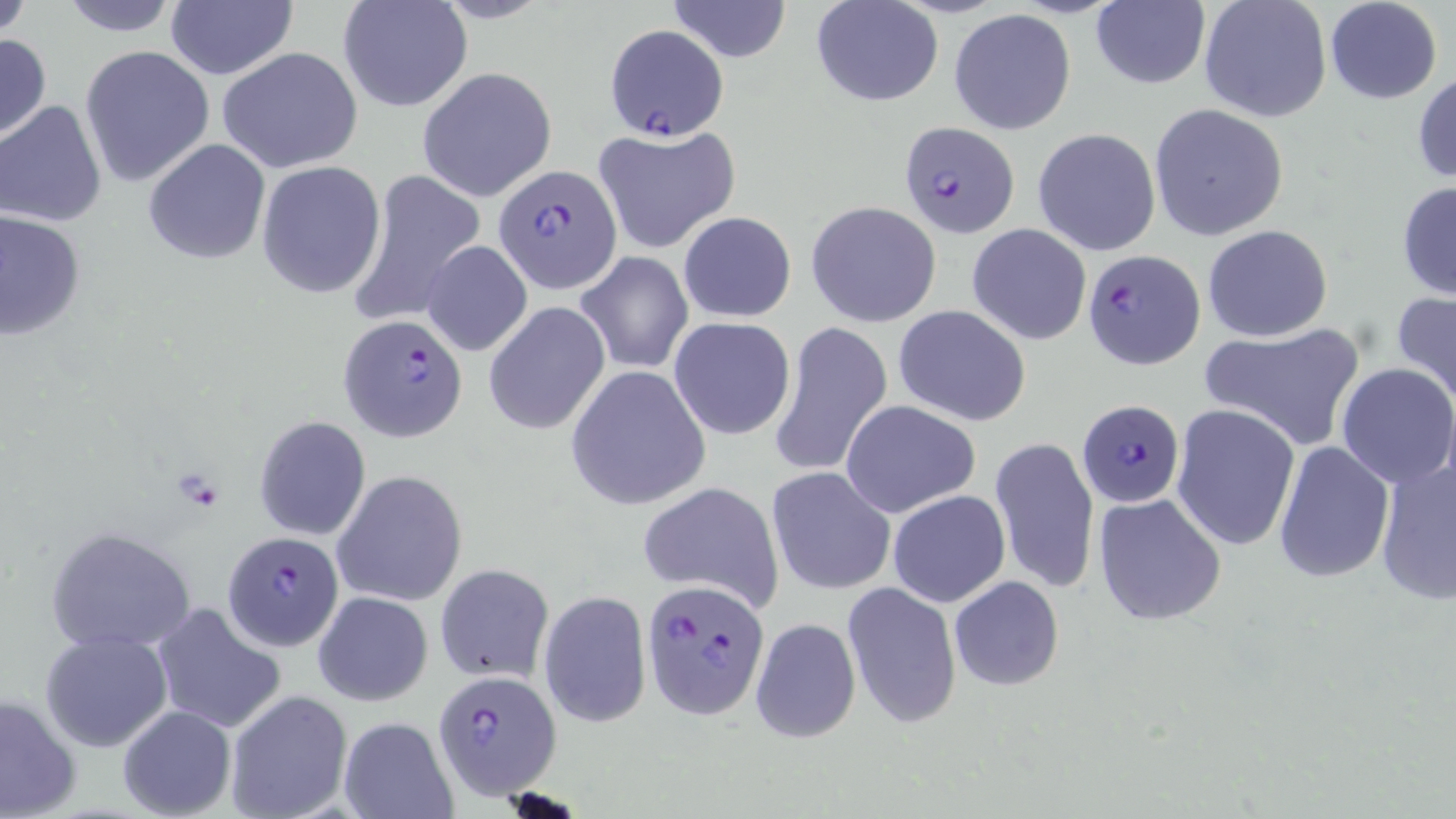

Approximate bounding boxes as (x1,y1)-(x2,y2) corner pairs in pixels. Platelet locations: (173,470)-(228,513). Uninfected red blood cell locations: (0,0)-(36,39), (54,0)-(186,37), (666,0)-(792,63), (812,0)-(943,106), (1198,0)-(1331,122), (1324,0)-(1442,104), (337,1)-(472,114), (1090,1)-(1209,90), (164,2)-(298,81), (949,8)-(1077,135), (0,34)-(50,142), (79,45)-(214,186), (216,46)-(366,174), (416,67)-(556,201), (1412,70)-(1456,186), (0,100)-(110,228), (1150,104)-(1289,241), (590,124)-(740,255), (1033,127)-(1162,257), (144,140)-(270,265), (256,161)-(387,298), (347,168)-(485,324), (1396,180)-(1456,303), (807,201)-(945,327), (1,209)-(85,341), (678,210)-(797,322), (966,223)-(1091,346), (1202,224)-(1333,342), (421,239)-(531,356), (575,251)-(692,374), (1391,290)-(1456,411), (484,301)-(610,434), (893,305)-(1033,426), (668,316)-(797,441), (769,321)-(892,480), (1199,324)-(1365,449), (1335,363)-(1456,488), (567,364)-(712,509), (840,399)-(981,519), (1171,403)-(1300,551), (253,416)-(371,541), (991,434)-(1099,597), (1273,440)-(1395,583), (1374,455)-(1456,605), (766,466)-(896,596), (332,470)-(468,607), (637,481)-(786,613), (887,490)-(1010,609), (1093,492)-(1226,626), (45,526)-(196,654), (435,563)-(555,684), (949,576)-(1064,691), (843,582)-(962,729), (538,590)-(651,727), (313,591)-(433,707), (151,603)-(287,736), (749,616)-(861,745), (40,629)-(172,753), (224,689)-(354,819), (1,692)-(81,819), (117,704)-(236,819), (337,716)-(458,819). Plasmodium falciparum-infected red blood cell locations: (604,25)-(725,138), (899,122)-(1019,239), (497,164)-(622,292), (1083,248)-(1204,369), (339,315)-(469,444), (1075,399)-(1185,509), (222,531)-(346,651), (640,580)-(770,721), (433,669)-(560,798). Slide-level diagnosis: Plasmodium falciparum. Light microscopy. May-Grünwald-Giemsa stain. Thin blood smear. 1000x magnification. Single field of view. Image is 1456×819 pixels.